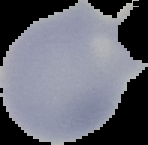
Result: no malaria parasites seen. Image is 148×145 pixels. From a thin blood smear. Cell region segmented out of the field of view; the surrounding area is masked to black.